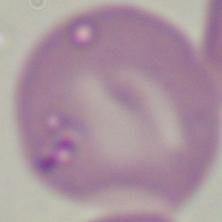
magnification: 1000x
identification: Babesia
modality: micrograph